Locate every Plasmodium parasite.
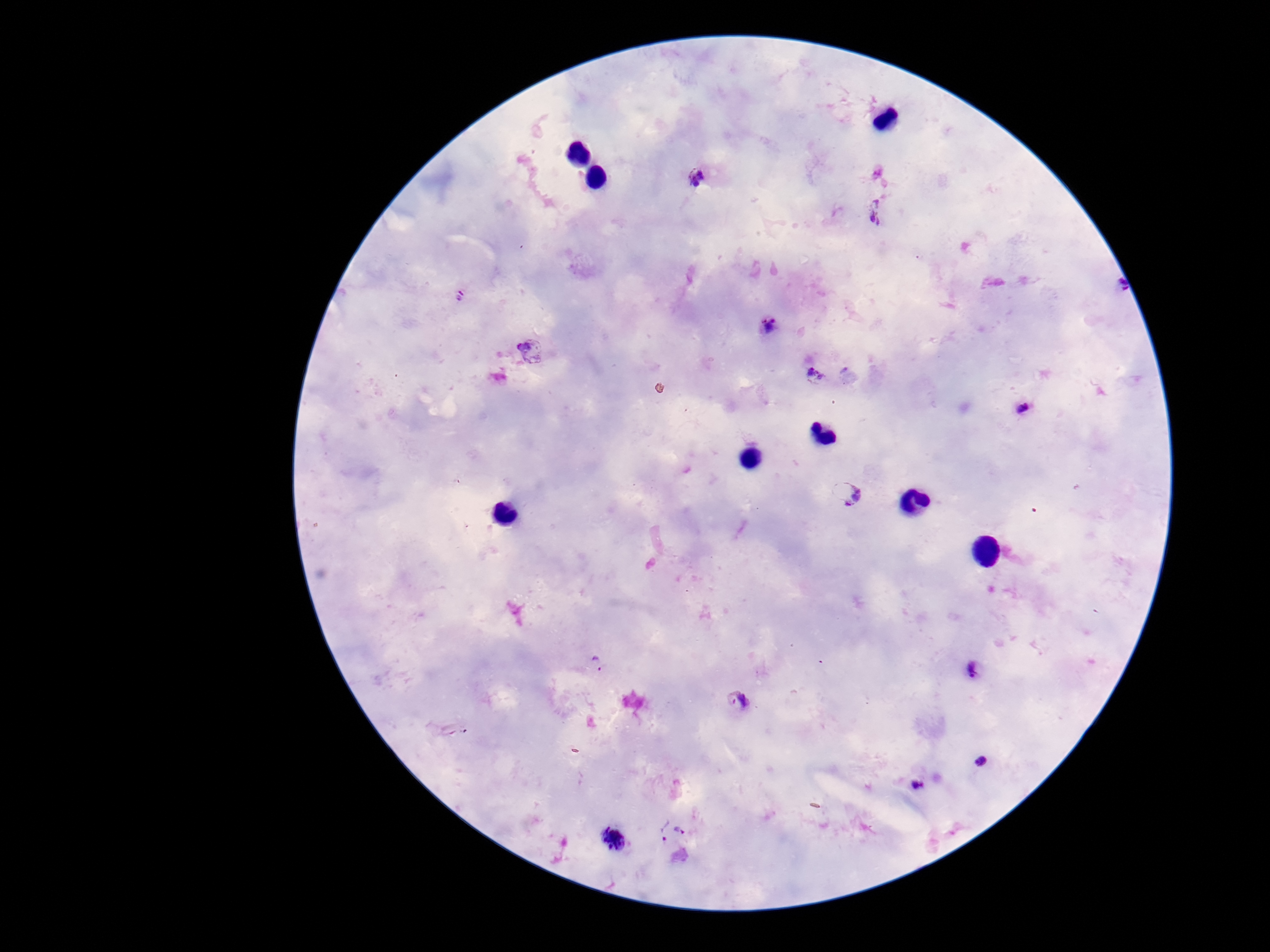

Approximate centers as {x, y} in pixels.
Plasmodium parasites: {697, 177}, {873, 213}, {1116, 288}, {458, 297}, {768, 326}, {532, 351}, {818, 378}, {1022, 409}, {849, 493}, {597, 663}, {972, 672}, {737, 701}, {982, 762}, {917, 785}, {662, 830}, {681, 830}, {615, 840}.

patient malaria status = positive
capture = smartphone camera through the microscope eyepiece
image size = 1270×952 pixels
stain = Giemsa
field of view = one from this slide
magnification = 100x
preparation = thick blood smear